Assess this cell for malaria.
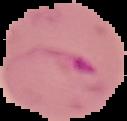
It is parasitized.

Summary:
  - Preparation: thin blood smear
  - Image type: segmented cell region with the area outside set to black
  - Image size: 127×121 pixels